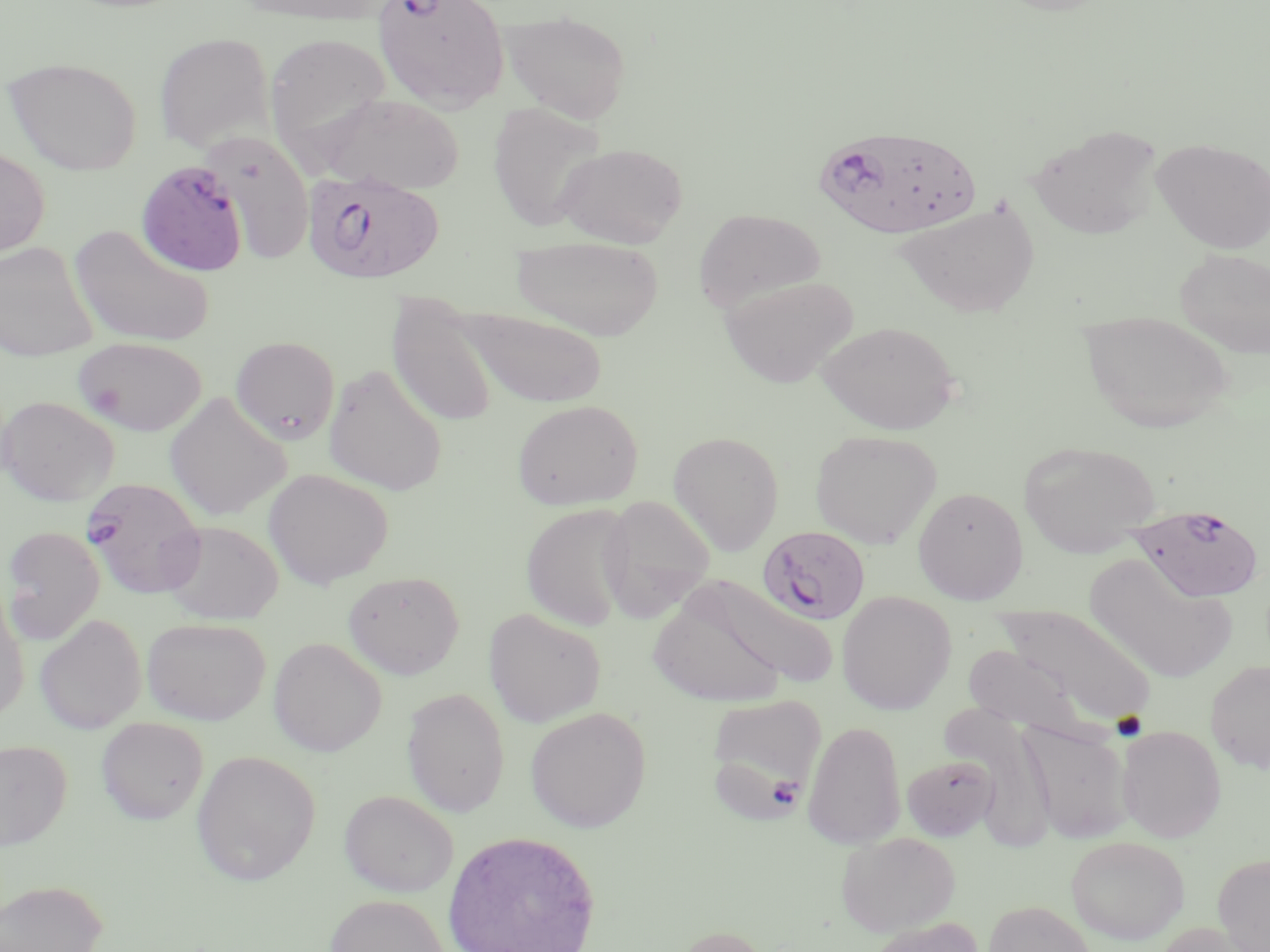

Approximate bounding boxes as named x1/y1/x2/y2 corners in pixels. Uninfected red blood cell locations: (x1=230, y1=0, x2=392, y2=26), (x1=990, y1=0, x2=1119, y2=16), (x1=499, y1=9, x2=633, y2=122), (x1=154, y1=32, x2=274, y2=153), (x1=265, y1=32, x2=393, y2=161), (x1=3, y1=55, x2=142, y2=176), (x1=316, y1=92, x2=465, y2=195), (x1=488, y1=102, x2=607, y2=233), (x1=1027, y1=123, x2=1163, y2=241), (x1=202, y1=131, x2=315, y2=266), (x1=1151, y1=138, x2=1270, y2=253), (x1=554, y1=142, x2=688, y2=248), (x1=0, y1=146, x2=50, y2=260), (x1=895, y1=197, x2=1042, y2=319), (x1=693, y1=208, x2=826, y2=313), (x1=68, y1=224, x2=215, y2=348), (x1=511, y1=235, x2=665, y2=340), (x1=0, y1=241, x2=98, y2=363), (x1=1174, y1=248, x2=1270, y2=358), (x1=720, y1=275, x2=858, y2=388), (x1=387, y1=293, x2=500, y2=429), (x1=458, y1=306, x2=607, y2=409), (x1=1079, y1=309, x2=1235, y2=433), (x1=817, y1=320, x2=961, y2=435), (x1=73, y1=336, x2=207, y2=436), (x1=230, y1=336, x2=340, y2=444), (x1=323, y1=364, x2=448, y2=496), (x1=163, y1=393, x2=291, y2=520), (x1=0, y1=395, x2=119, y2=506), (x1=512, y1=399, x2=643, y2=511), (x1=810, y1=429, x2=943, y2=549), (x1=667, y1=430, x2=785, y2=556), (x1=1019, y1=439, x2=1162, y2=558), (x1=263, y1=469, x2=394, y2=589), (x1=912, y1=485, x2=1028, y2=604), (x1=598, y1=494, x2=717, y2=620), (x1=520, y1=502, x2=635, y2=631), (x1=161, y1=520, x2=284, y2=625), (x1=2, y1=526, x2=105, y2=644), (x1=1083, y1=555, x2=1237, y2=684), (x1=343, y1=570, x2=464, y2=679), (x1=691, y1=574, x2=840, y2=690), (x1=646, y1=586, x2=789, y2=706), (x1=837, y1=590, x2=957, y2=714), (x1=0, y1=591, x2=29, y2=723), (x1=992, y1=602, x2=1157, y2=731), (x1=483, y1=608, x2=606, y2=727), (x1=34, y1=613, x2=147, y2=733), (x1=142, y1=617, x2=271, y2=724), (x1=268, y1=636, x2=387, y2=756), (x1=962, y1=643, x2=1092, y2=739), (x1=1205, y1=660, x2=1270, y2=772), (x1=402, y1=687, x2=510, y2=817), (x1=708, y1=692, x2=830, y2=790), (x1=525, y1=706, x2=651, y2=833), (x1=96, y1=717, x2=209, y2=825), (x1=1020, y1=719, x2=1133, y2=844), (x1=803, y1=720, x2=906, y2=849), (x1=1117, y1=724, x2=1227, y2=842), (x1=0, y1=739, x2=71, y2=850), (x1=191, y1=750, x2=321, y2=885), (x1=902, y1=754, x2=999, y2=841), (x1=340, y1=789, x2=459, y2=897), (x1=441, y1=830, x2=601, y2=952), (x1=837, y1=831, x2=961, y2=937), (x1=1066, y1=834, x2=1189, y2=944), (x1=1213, y1=853, x2=1270, y2=951), (x1=0, y1=879, x2=107, y2=952), (x1=323, y1=894, x2=452, y2=952), (x1=984, y1=900, x2=1095, y2=951), (x1=864, y1=916, x2=985, y2=952), (x1=1153, y1=921, x2=1257, y2=952), (x1=673, y1=924, x2=772, y2=952). Plasmodium falciparum-infected red blood cell locations: (x1=371, y1=0, x2=511, y2=112), (x1=812, y1=121, x2=984, y2=240), (x1=134, y1=158, x2=248, y2=280), (x1=302, y1=170, x2=445, y2=285), (x1=81, y1=476, x2=207, y2=599), (x1=1122, y1=505, x2=1262, y2=603), (x1=756, y1=526, x2=869, y2=625). Slide-level diagnosis: Plasmodium falciparum. Light microscopy. Image is 1270×952 pixels. May-Grünwald-Giemsa stain. Single field of view. Thin blood film. Captured at 1000x magnification.